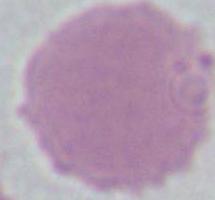
Summary:
  - Magnification: 1000x
  - Modality: micrograph
  - Identification: erythrocyte